Locate every blood parasite and identify its species.
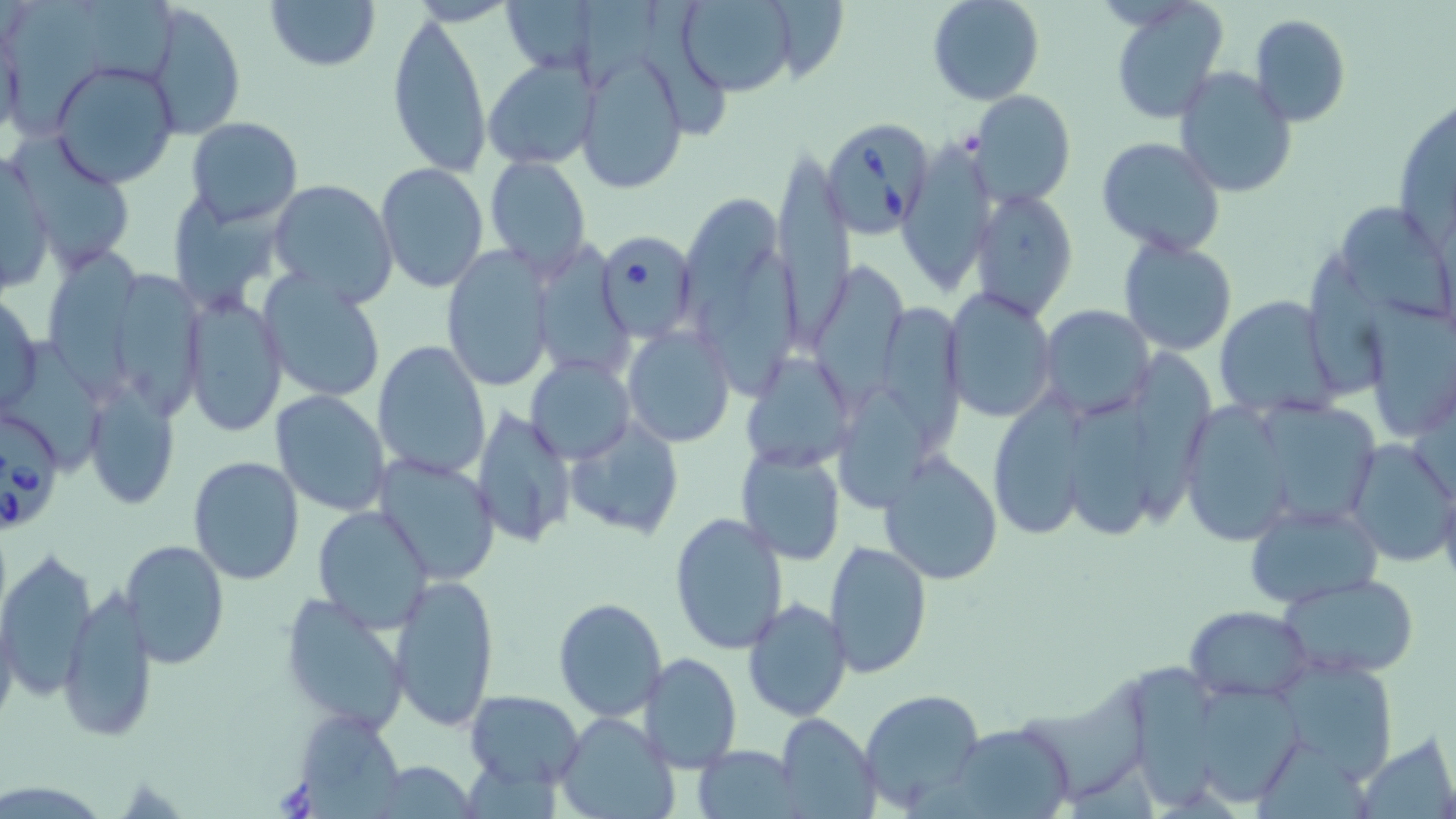

Approximate bounding boxes as (x1,y1)-(x2,y2) corner pairs in pixels.
Babesia divergens-infected red blood cells: (823,114)-(938,241), (605,230)-(696,335), (2,413)-(61,536).
No Plasmodium falciparum, Plasmodium ovale, Plasmodium malariae, Plasmodium vivax, or Trypanosoma brucei observed.

{
  "slide_level_diagnosis": "Babesia divergens",
  "stain": "May-Grünwald-Giemsa",
  "modality": "optical microscopy",
  "preparation": "thin blood film",
  "magnification": "1000x",
  "uninfected_red_blood_cell_locations": "approximate bounding boxes as (x1,y1)-(x2,y2) corner pairs in pixels: (262,0)-(381,73), (674,0)-(803,97), (926,0)-(1045,106), (1110,1)-(1229,121), (148,2)-(247,137), (643,2)-(736,134), (7,4)-(109,133), (387,10)-(492,179), (1248,13)-(1350,127), (575,51)-(688,196), (483,57)-(597,170), (50,60)-(179,188), (1173,69)-(1297,199), (969,90)-(1077,207), (185,117)-(303,226), (15,130)-(133,268), (898,136)-(997,292), (1095,138)-(1225,257), (770,146)-(854,342), (0,150)-(54,300), (484,157)-(592,273), (374,162)-(489,295), (267,178)-(399,305), (969,189)-(1078,321), (682,193)-(782,340), (1338,198)-(1453,326), (1119,237)-(1236,355), (527,242)-(635,383), (438,248)-(558,391), (44,250)-(142,401), (702,256)-(802,391), (817,260)-(918,413), (113,268)-(201,410), (258,272)-(387,403), (943,289)-(1058,422), (1,290)-(43,416), (184,294)-(288,438), (1213,294)-(1344,420), (887,301)-(971,447), (1363,301)-(1456,440), (1038,304)-(1155,419), (622,323)-(736,447), (372,339)-(492,482), (746,346)-(862,469), (1135,350)-(1225,530), (527,356)-(634,464), (85,379)-(181,509), (843,383)-(928,503), (1068,387)-(1168,540), (1262,389)-(1379,521), (270,390)-(392,516), (985,390)-(1099,539), (1181,401)-(1296,545), (471,404)-(575,549), (567,418)-(685,541), (1343,438)-(1455,567), (735,446)-(847,565), (878,454)-(1003,587), (188,455)-(306,587), (377,455)-(502,585), (1243,500)-(1384,607), (313,504)-(434,632), (669,511)-(789,656), (122,539)-(230,669), (825,541)-(932,678), (0,547)-(97,700), (390,572)-(500,730), (1277,572)-(1422,679), (59,589)-(158,740), (279,593)-(412,733), (741,596)-(852,723), (553,597)-(667,721), (1185,606)-(1312,702), (640,654)-(743,772), (1275,656)-(1401,781), (1129,658)-(1218,808), (1025,674)-(1163,803), (1202,683)-(1307,800), (466,690)-(585,787), (859,690)-(984,811), (299,712)-(399,819), (773,713)-(879,818), (553,714)-(677,819), (951,722)-(1069,819), (693,745)-(801,818), (372,762)-(477,815)",
  "field_of_view": "single",
  "image_size": "1456×819 pixels"
}